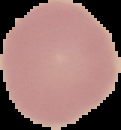 From a thin blood smear. Result: no malaria parasites seen. Image is 121×130 pixels. Segmented cell region on a black background.